Point out each leukocyte.
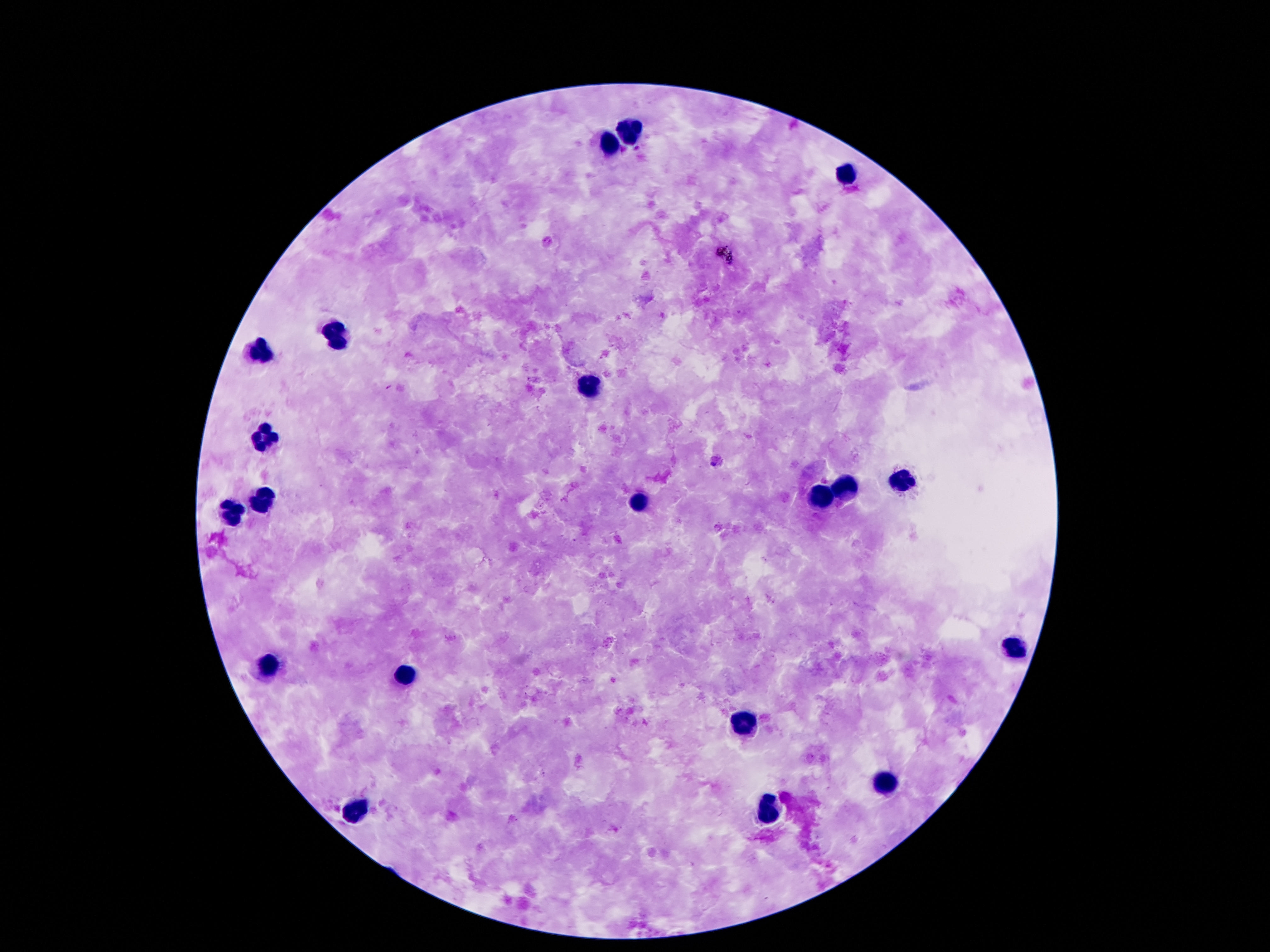
Approximate centers as (x, y) in pixels.
Leukocytes: (632, 132), (611, 144), (846, 174), (338, 337), (262, 354), (588, 386), (271, 434), (905, 483), (846, 489), (267, 499), (817, 499), (642, 504), (237, 511), (1018, 649), (269, 668), (403, 676), (747, 724), (884, 783), (359, 810), (770, 812).

magnification = 100x
patient malaria status = not infected
stain = Giemsa
capture = smartphone camera through the microscope eyepiece
preparation = thick peripheral-blood smear
image size = 1270×952 pixels
field of view = one from this slide